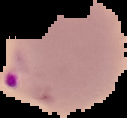

Result: Plasmodium parasites identified. From a thin blood smear. Image is 127×118 pixels. Cell region segmented out of the field of view; the surrounding area is masked to black.